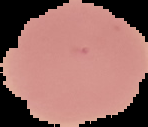

image_type: segmented cell region with the area outside set to black
image_size: 148×127 pixels
preparation: thin blood smear
result: no Plasmodium parasites seen